Give the extent of all uninfected red blood cells.
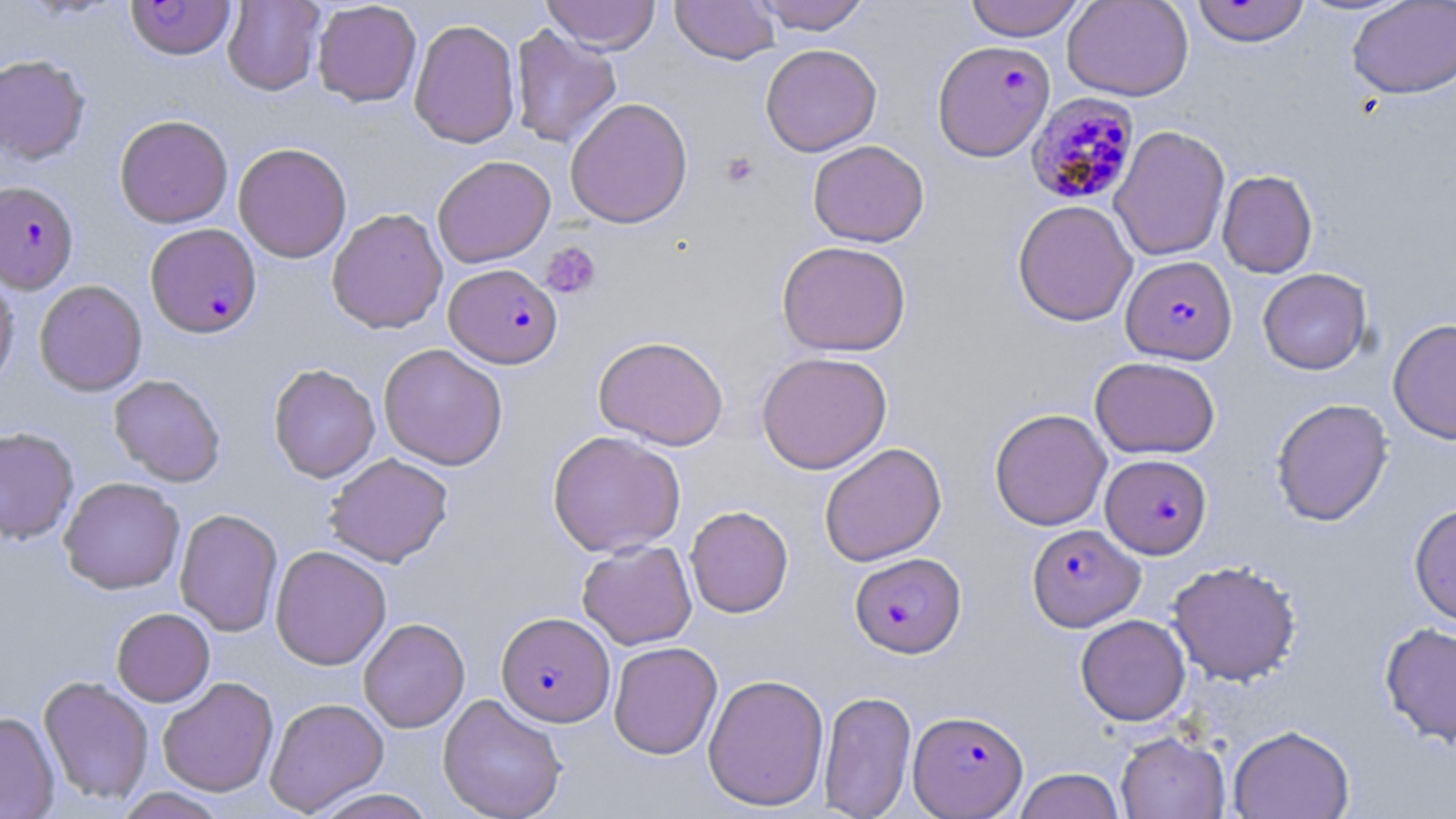
Approximate bounding boxes as (x1, y1, x2, y2) in pixels.
Uninfected red blood cells: (223, 0, 325, 96), (541, 0, 661, 53), (670, 0, 781, 64), (753, 0, 871, 34), (964, 0, 1087, 41), (1062, 0, 1194, 101), (1190, 0, 1311, 47), (312, 1, 422, 107), (1347, 1, 1456, 99), (408, 18, 521, 149), (509, 23, 622, 149), (760, 43, 882, 156), (0, 55, 91, 164), (564, 97, 693, 228), (114, 114, 234, 228), (1110, 125, 1230, 261), (808, 140, 929, 247), (233, 142, 352, 263), (432, 155, 555, 268), (1217, 170, 1318, 278), (1012, 199, 1138, 327), (326, 207, 448, 334), (777, 240, 911, 356), (0, 266, 19, 394), (1258, 268, 1371, 375), (34, 279, 147, 396), (1388, 318, 1456, 444), (593, 335, 729, 450), (378, 343, 508, 470), (756, 351, 892, 474), (1090, 356, 1220, 459), (268, 363, 380, 483), (108, 374, 226, 487), (1271, 398, 1393, 526), (989, 408, 1111, 531), (0, 427, 79, 543), (547, 430, 686, 557), (819, 442, 947, 566), (324, 452, 453, 567), (59, 477, 185, 595), (1409, 503, 1456, 627), (685, 505, 794, 618), (174, 508, 283, 637), (577, 540, 697, 650), (270, 545, 391, 670), (1167, 560, 1302, 685), (111, 608, 215, 706), (1075, 614, 1191, 726), (358, 618, 469, 733), (1379, 622, 1456, 746), (608, 641, 723, 759), (703, 673, 829, 811), (38, 676, 154, 805), (157, 676, 279, 797), (818, 689, 917, 819), (438, 693, 567, 819), (265, 698, 389, 815), (0, 711, 60, 818), (1228, 724, 1355, 819), (1115, 731, 1230, 818), (1013, 768, 1125, 818), (113, 788, 229, 819), (307, 788, 439, 818).

slide-level diagnosis = Plasmodium falciparum
field of view = single
Plasmodium falciparum-infected red blood cell locations = approximate bounding boxes as (x1, y1, x2, y2) in pixels: (125, 0, 239, 58), (932, 39, 1055, 161), (1025, 92, 1140, 205), (0, 180, 79, 293), (145, 223, 262, 338), (1120, 256, 1237, 365), (444, 263, 562, 368), (1101, 454, 1211, 558), (1027, 523, 1144, 631), (849, 552, 966, 657), (496, 611, 615, 726), (908, 709, 1028, 817)
modality = light microscopy
preparation = thin blood smear
stain = May-Grünwald-Giemsa
image size = 1456×819 pixels
magnification = 1000x
platelet locations = approximate bounding boxes as (x1, y1, x2, y2) in pixels: (721, 151, 758, 188), (540, 242, 602, 299)